Name the blood parasite species.
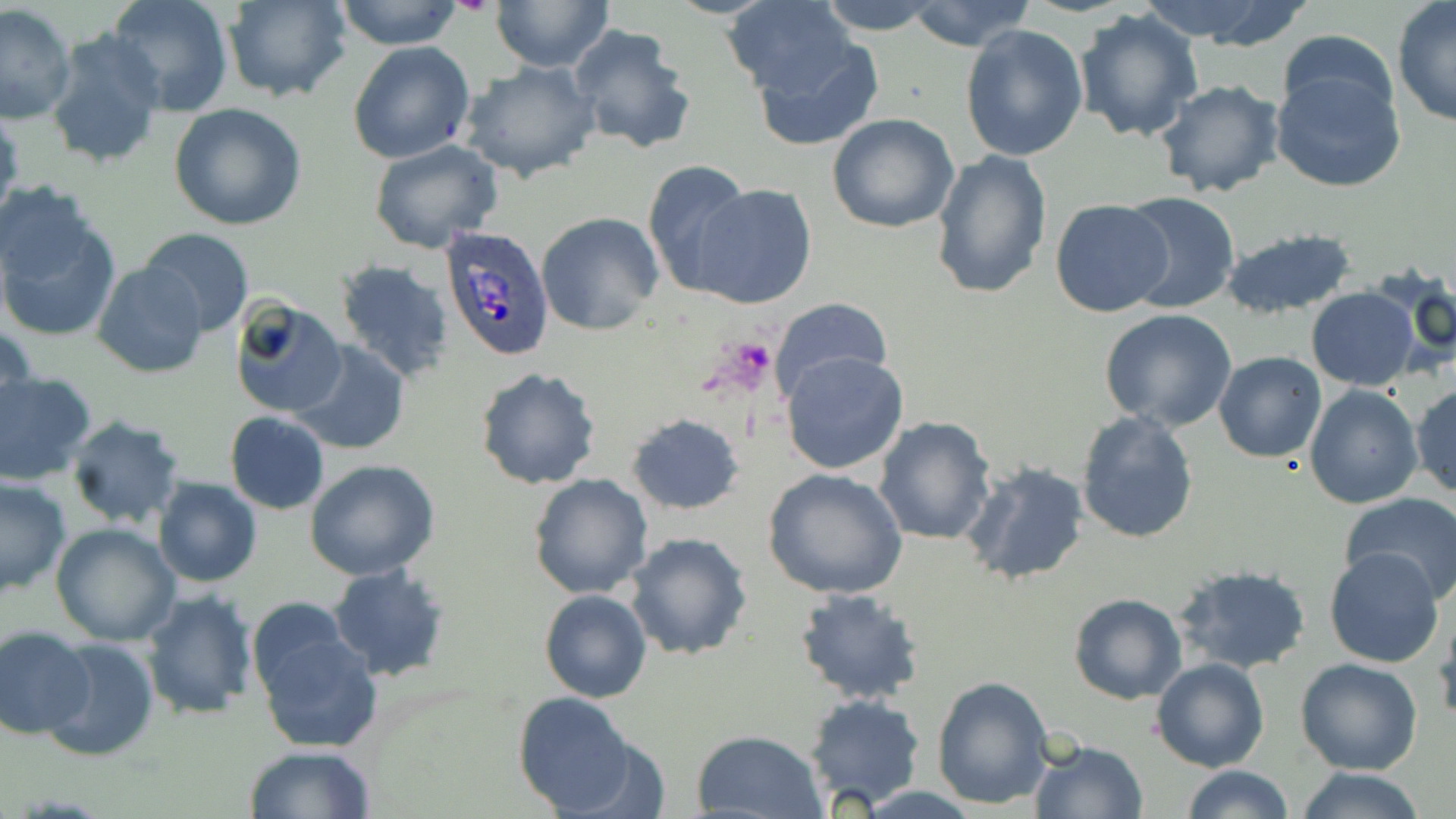
Plasmodium ovale.

Approximate bounding boxes as [x1, y1, x2, y2] in pixels. Uninfected red blood cell locations: [106, 0, 232, 116], [223, 0, 349, 102], [333, 0, 464, 49], [491, 0, 614, 73], [720, 0, 862, 101], [816, 0, 942, 35], [904, 1, 1035, 52], [1170, 2, 1318, 51], [1391, 3, 1456, 128], [1, 5, 76, 124], [1074, 8, 1204, 142], [567, 23, 697, 155], [961, 24, 1089, 161], [44, 26, 169, 172], [1275, 31, 1402, 133], [749, 33, 884, 151], [348, 42, 475, 164], [458, 60, 602, 183], [1270, 65, 1406, 194], [1153, 79, 1286, 199], [169, 103, 307, 231], [0, 105, 23, 228], [827, 112, 960, 234], [369, 139, 505, 255], [931, 149, 1053, 300], [642, 158, 753, 295], [691, 183, 818, 310], [0, 189, 120, 340], [1118, 191, 1239, 314], [1050, 198, 1176, 318], [537, 211, 665, 335], [1221, 226, 1360, 320], [139, 227, 254, 338], [333, 260, 455, 384], [93, 261, 208, 379], [1378, 267, 1456, 371], [1306, 287, 1420, 389], [768, 297, 893, 399], [228, 298, 347, 420], [1099, 308, 1237, 432], [1, 320, 36, 433], [291, 340, 410, 455], [781, 351, 909, 475], [1213, 351, 1326, 462], [474, 367, 603, 490], [0, 371, 96, 486], [1410, 379, 1456, 499], [1304, 383, 1423, 509], [1076, 410, 1199, 543], [224, 411, 329, 516], [626, 413, 745, 515], [873, 416, 997, 544], [65, 417, 187, 530], [303, 460, 442, 582], [960, 461, 1091, 587], [763, 468, 908, 600], [529, 474, 652, 598], [0, 477, 71, 596], [151, 477, 263, 588], [1338, 493, 1456, 605], [50, 523, 181, 645], [624, 532, 753, 661], [1324, 548, 1444, 668], [328, 562, 451, 682], [1173, 565, 1313, 675], [140, 589, 260, 719], [538, 590, 651, 703], [793, 590, 926, 705], [1068, 593, 1186, 705], [246, 596, 352, 701], [1433, 611, 1455, 728], [251, 621, 384, 754], [0, 627, 94, 738], [39, 634, 160, 761], [1152, 657, 1270, 771], [1296, 657, 1422, 774], [932, 676, 1056, 810], [513, 692, 634, 816], [802, 692, 927, 810], [691, 730, 827, 818], [1028, 740, 1149, 819], [244, 745, 377, 819], [1183, 765, 1294, 819], [1293, 766, 1425, 819]. Plasmodium ovale-infected red blood cell locations: [438, 226, 555, 360]. Platelet locations: [717, 338, 776, 388]. Light microscopy. Image is 1456×819 pixels. May-Grünwald-Giemsa-stained preparation. Single field of view. Captured at 1000x magnification. Thin blood smear.